Assess the morphology of the erythrocytes.
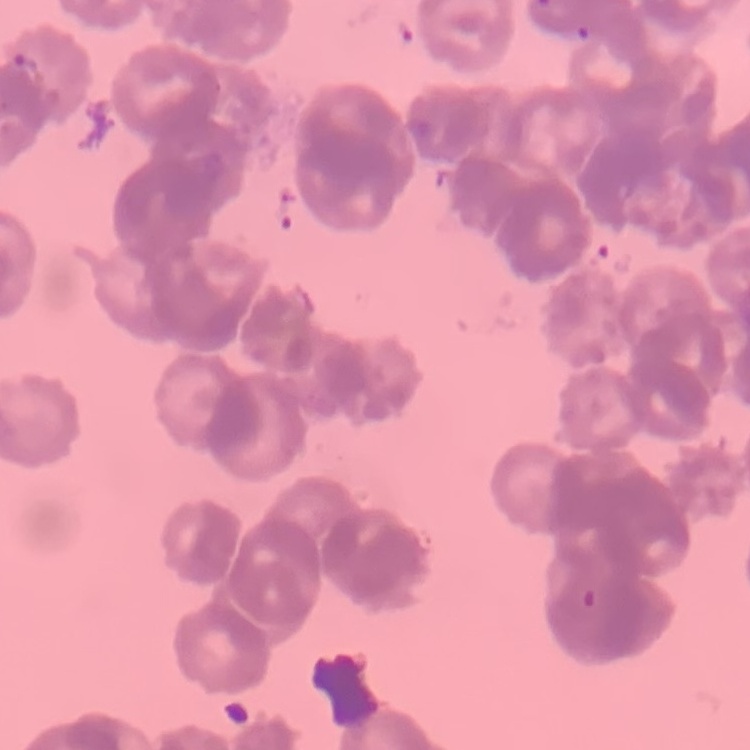
They show rouleaux formation.

Thin blood smear. Stained with either Field's or Giemsa. One tile cut from a larger photomicrograph.